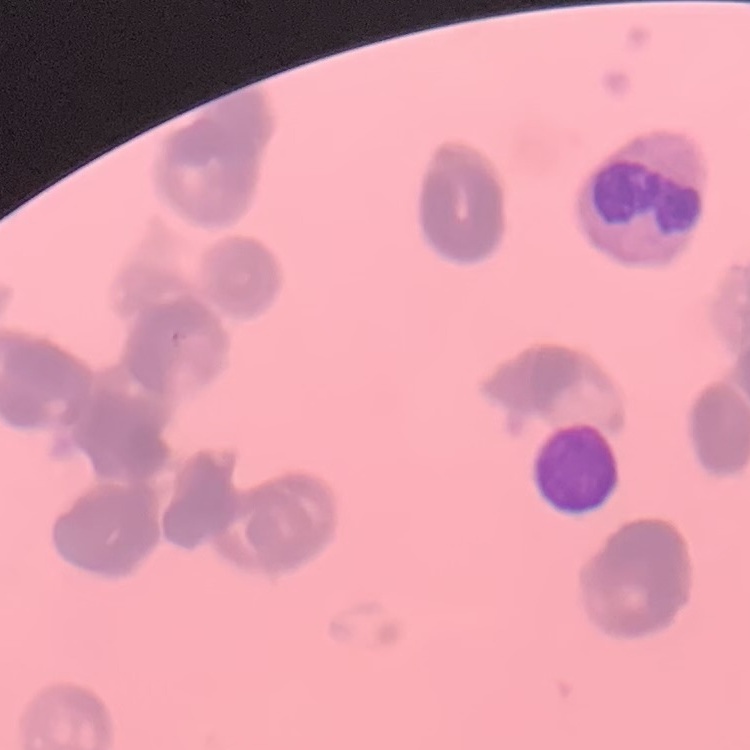
The red blood cells show rouleaux formation. Field's or Giemsa stain. Square crop of a larger photomicrograph. Thin peripheral smear.